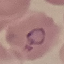
Malaria status: parasitized. Automatically extracted cell patch, resized to 64 × 64 pixels. Photographed with a smartphone camera at the microscope eyepiece. Thin blood smear. Giemsa-stained preparation.